State which parasite is depicted.
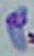
This is Toxoplasma gondii.

modality = photomicrograph
magnification = 1000x